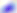 400x magnification. Micrograph. Toxoplasma gondii is shown.